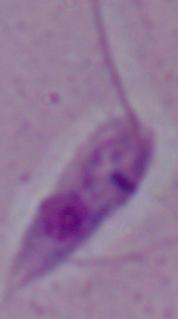

Summary:
  - Identification: Leishmania
  - Modality: photomicrograph
  - Magnification: 1000x